Name the blood parasite species.
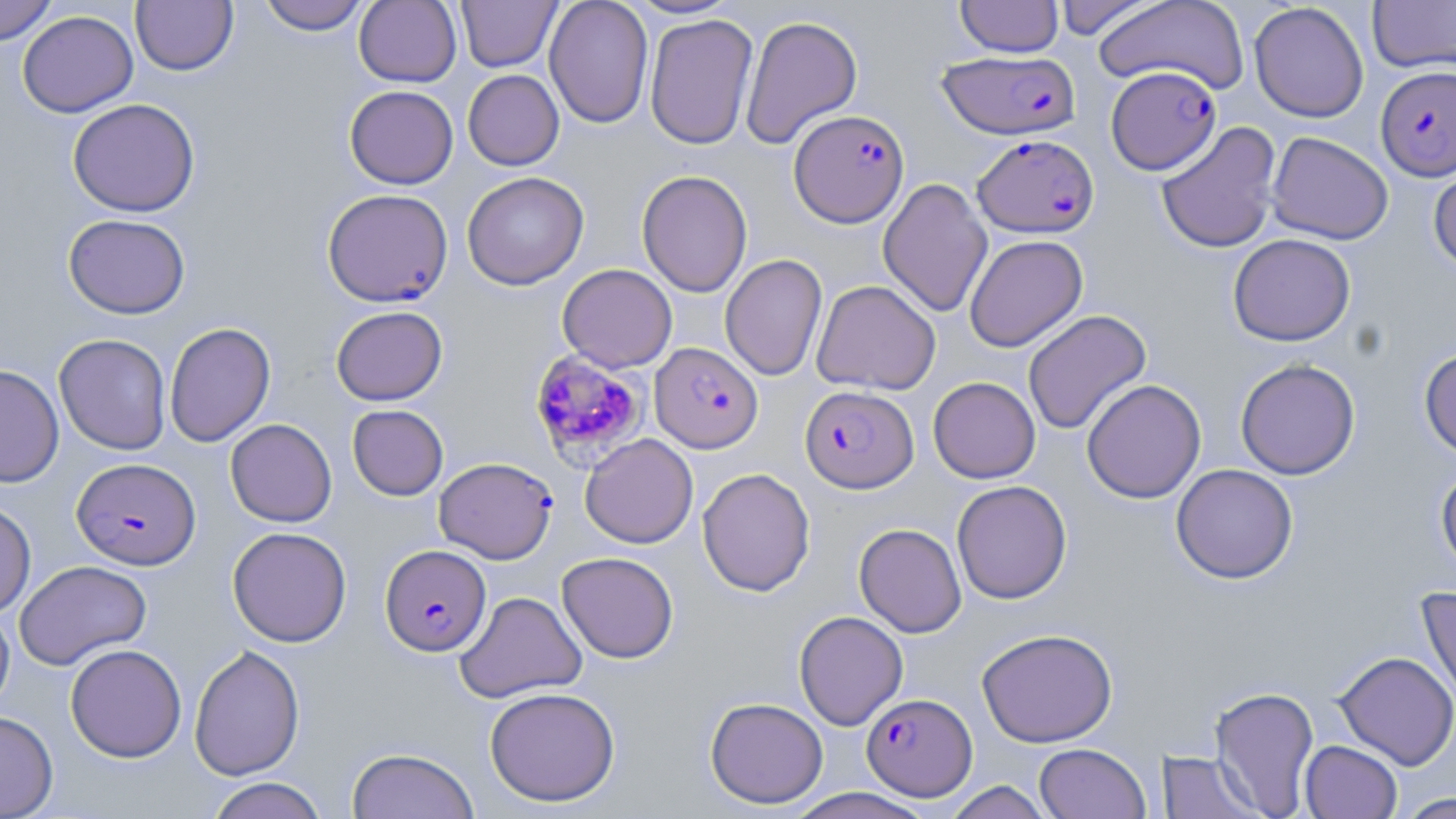
Plasmodium falciparum.

Approximate bounding boxes as (x1,y1)-(x2,y2) corner pairs in pixels. Uninfected red blood cell locations: (0,0)-(57,46), (257,0)-(370,35), (354,0)-(461,87), (544,0)-(654,129), (623,0)-(743,19), (955,0)-(1064,57), (1052,0)-(1160,40), (1094,0)-(1249,95), (1367,0)-(1456,75), (130,1)-(238,75), (456,1)-(561,72), (1249,2)-(1369,122), (17,10)-(138,117), (644,13)-(758,150), (740,15)-(863,149), (463,69)-(564,170), (344,85)-(458,189), (67,98)-(200,217), (1156,121)-(1282,254), (1267,131)-(1394,245), (1429,158)-(1456,273), (636,170)-(753,297), (461,171)-(589,290), (878,177)-(993,319), (63,213)-(190,318), (1228,233)-(1355,346), (964,234)-(1087,352), (720,254)-(828,382), (557,263)-(677,372), (812,279)-(941,395), (331,305)-(448,405), (1022,309)-(1151,435), (164,322)-(276,447), (53,333)-(172,455), (1419,347)-(1456,458), (1235,358)-(1361,480), (0,365)-(64,488), (928,376)-(1041,483), (1081,378)-(1206,503), (347,404)-(448,500), (225,418)-(337,527), (580,433)-(698,548), (1171,463)-(1298,584), (1435,464)-(1456,578), (697,467)-(815,597), (951,480)-(1072,604), (0,500)-(36,618), (854,523)-(967,638), (227,526)-(351,647), (557,551)-(679,663), (14,560)-(152,670), (1416,587)-(1456,711), (454,590)-(587,703), (0,604)-(14,716), (793,611)-(908,730), (977,628)-(1118,748), (65,643)-(186,762), (189,644)-(305,780), (1333,651)-(1456,770), (485,686)-(620,807), (1208,686)-(1320,816), (705,696)-(828,809), (0,711)-(58,818), (1299,740)-(1403,819), (1034,743)-(1151,819), (347,747)-(479,819), (1157,750)-(1265,818), (205,777)-(329,819), (942,781)-(1055,818), (783,788)-(935,819), (1393,792)-(1455,818). Plasmodium falciparum-infected red blood cell locations: (938,50)-(1080,139), (1106,65)-(1220,175), (1376,65)-(1456,181), (789,109)-(909,228), (972,134)-(1099,237), (322,188)-(453,307), (650,342)-(763,453), (531,351)-(650,467), (799,385)-(918,493), (434,456)-(558,563), (72,458)-(200,570), (380,544)-(491,656), (861,693)-(977,800). Single field of view. Thin blood film. May-Grünwald-Giemsa-stained preparation. Image is 1456×819 pixels. 1000x magnification. Optical microscopy.